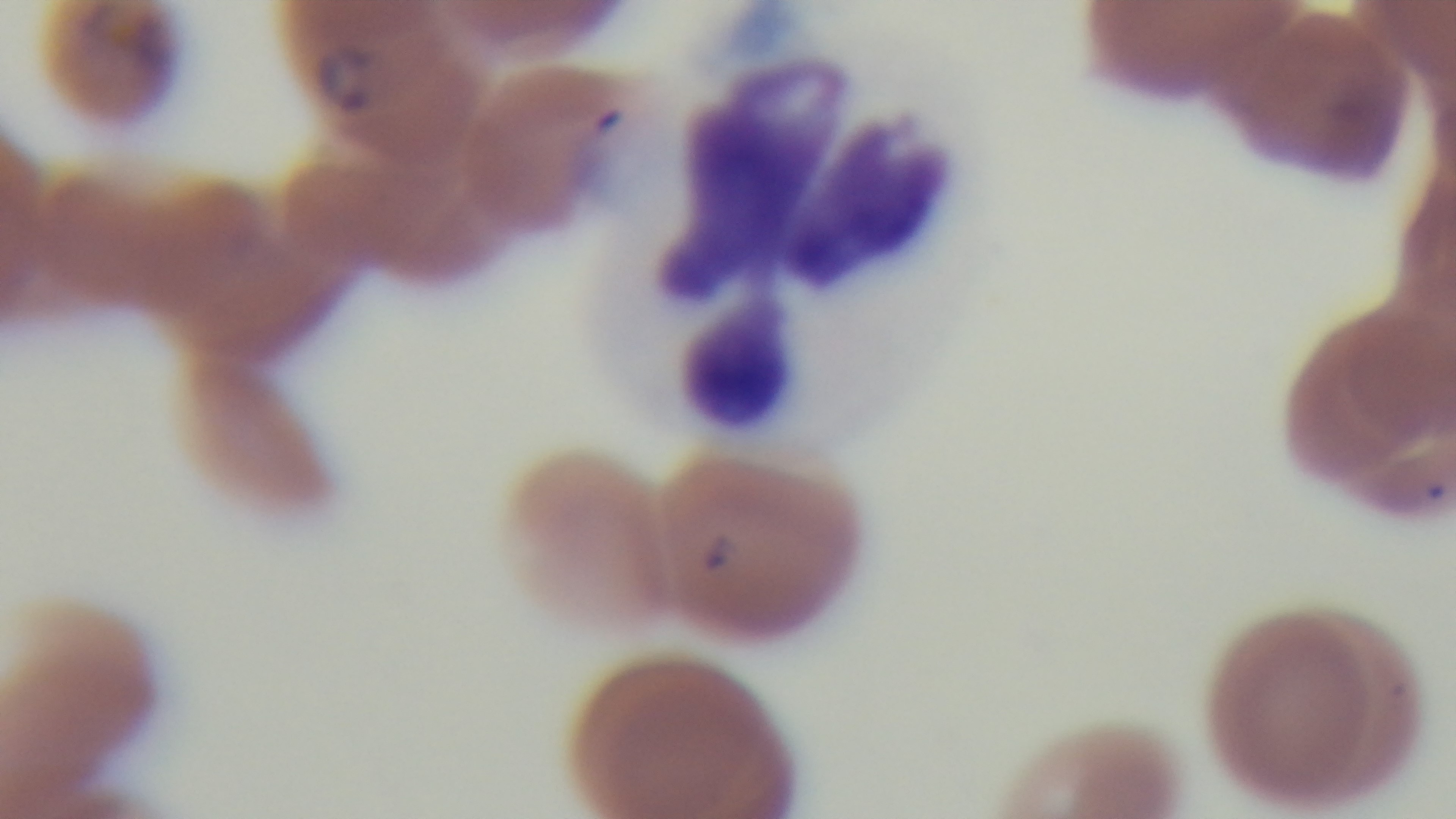
Giemsa stain. Malaria status: positive. Mounted 4K digital camera. Preparation: thin. Photomicrograph. 100x oil-immersion objective. Single field of view.